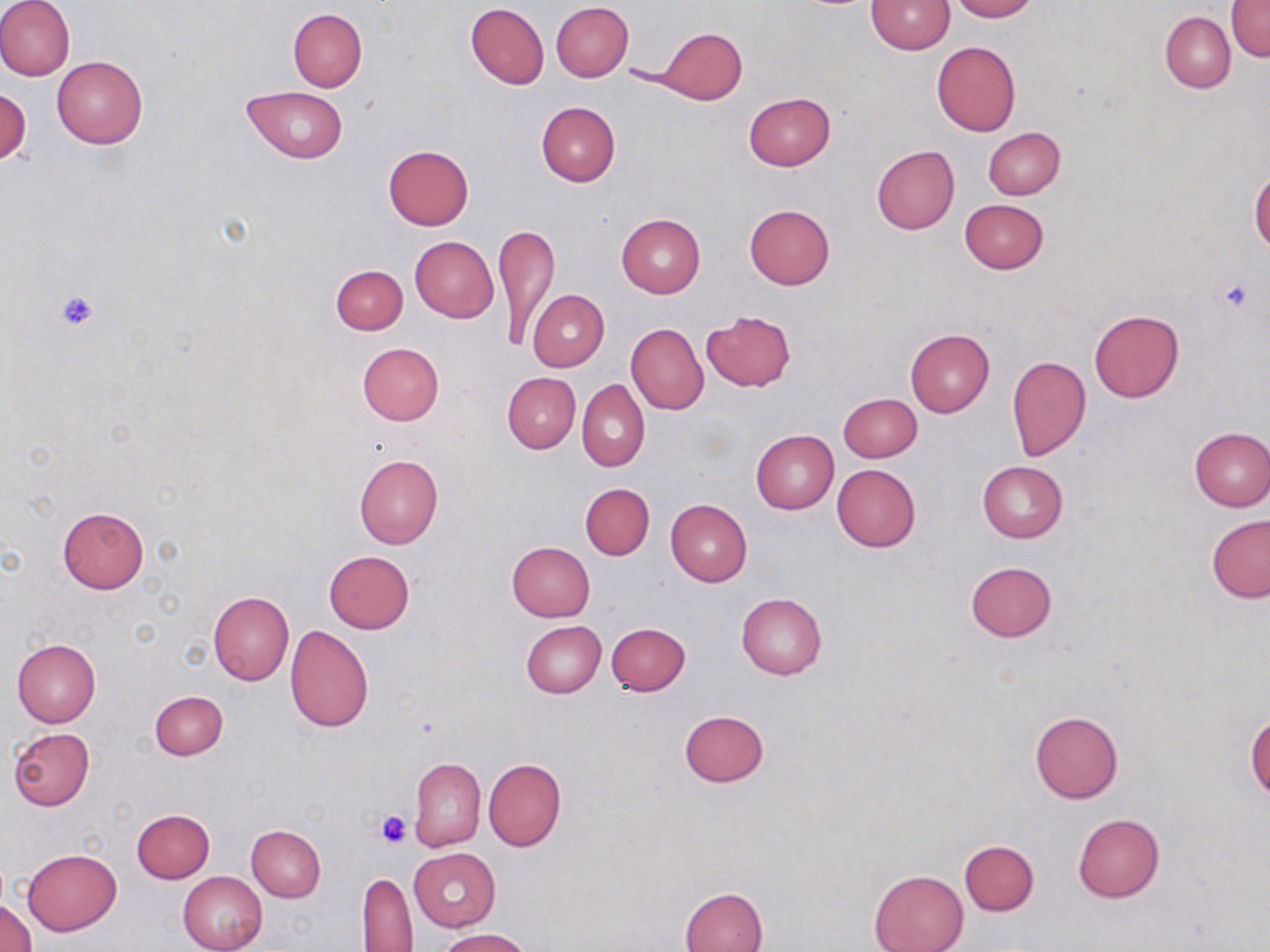
Approximate bounding boxes as [x1, y1, x2, y2] in pixels. Uninfected red blood cell locations: [0, 0, 76, 81], [948, 0, 1036, 21], [866, 1, 954, 54], [1227, 1, 1270, 63], [550, 2, 633, 82], [465, 3, 549, 88], [288, 8, 367, 91], [1161, 12, 1235, 92], [657, 26, 747, 104], [931, 41, 1020, 136], [51, 55, 148, 148], [1, 86, 31, 168], [242, 86, 349, 161], [744, 92, 835, 170], [535, 101, 620, 186], [983, 127, 1064, 199], [383, 145, 474, 230], [872, 145, 959, 234], [1250, 169, 1270, 256], [959, 199, 1049, 274], [744, 205, 835, 290], [616, 214, 706, 297], [496, 225, 559, 351], [409, 236, 498, 322], [331, 264, 408, 335], [527, 289, 609, 372], [1089, 308, 1185, 403], [701, 310, 796, 391], [626, 322, 708, 415], [905, 330, 994, 417], [357, 343, 443, 426], [1006, 355, 1091, 461], [503, 372, 581, 453], [576, 380, 650, 472], [837, 393, 921, 462], [1188, 426, 1270, 511], [751, 430, 839, 514], [354, 455, 443, 549], [976, 460, 1068, 542], [832, 464, 921, 551], [580, 482, 655, 560], [665, 499, 753, 587], [58, 506, 149, 593], [1206, 515, 1270, 603], [507, 542, 595, 622], [324, 550, 414, 633], [965, 561, 1057, 641], [209, 590, 293, 686], [736, 592, 827, 680], [520, 620, 606, 698], [605, 623, 690, 696], [284, 625, 374, 732], [12, 637, 101, 727], [150, 691, 227, 759], [679, 710, 770, 787], [1029, 711, 1123, 803], [1245, 712, 1270, 801], [8, 728, 95, 810], [410, 757, 485, 851], [484, 758, 566, 852], [131, 809, 214, 883], [1073, 813, 1164, 902], [247, 825, 326, 902], [959, 841, 1038, 915], [408, 848, 500, 930], [23, 849, 121, 935], [868, 870, 968, 952], [178, 871, 268, 952], [356, 873, 417, 950], [680, 887, 768, 952], [1, 897, 36, 952], [435, 928, 532, 951]. Platelet locations: [1215, 275, 1260, 318], [53, 288, 100, 332], [374, 809, 412, 848]. Slide-level diagnosis: no evidence of blood parasites. Thin blood film. 1000x magnification. Image is 1270×952 pixels. Light microscopy. May-Grünwald-Giemsa stain. One field of a larger specimen.